Report the malaria status of this cell.
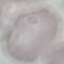
Uninfected.

Summary:
  - Capture: smartphone through the microscope eyepiece
  - Stain: Giemsa
  - Preparation: thin blood film
  - Image type: automatically extracted cell patch, resized to 64 × 64 pixels